State which parasite is depicted.
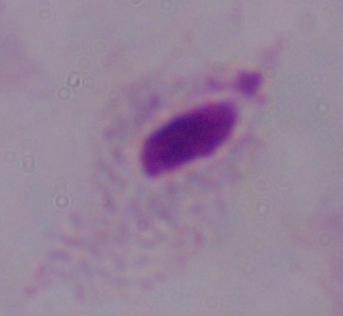

This is a trichomonad.

Summary:
  - Magnification: 1000x
  - Modality: photomicrograph